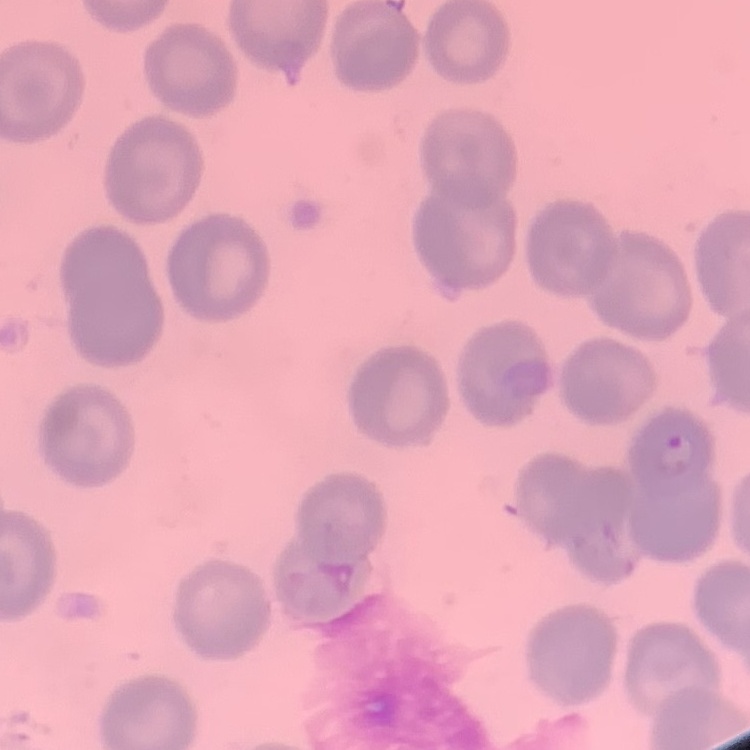 The erythrocytes show no rouleaux formation. One tile cut from a larger photomicrograph. Stained with either Field's or Giemsa. Thin blood smear.